Report the malaria status of this cell.
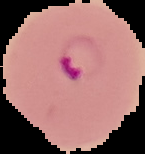

Parasitized.

image_size: 145×154 pixels
preparation: thin blood smear
image_type: segmented cell region on a black background